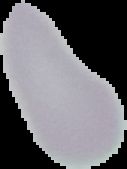 From a thin blood smear. Segmented cell region on a black background. Image is 127×169 pixels. Malaria status: uninfected.